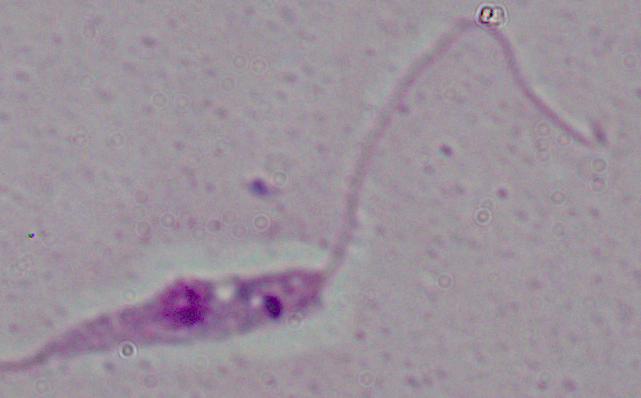
Summary:
  - Magnification: 1000x
  - Modality: photomicrograph
  - Identification: Leishmania